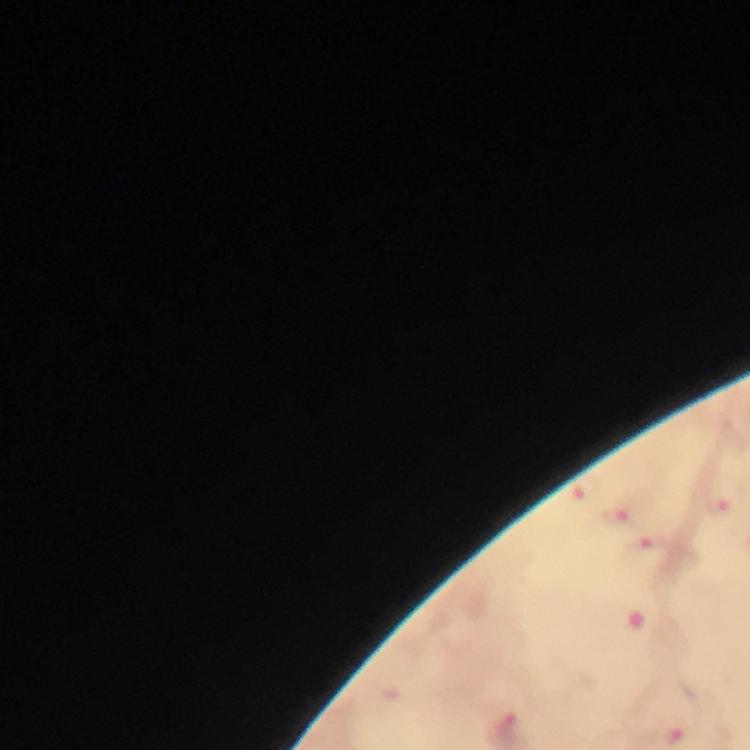
Approximate centers as (x, y) in pixels. Malaria parasite locations: (583, 490), (724, 507), (616, 516), (654, 548). Giemsa stain. Image is 750×750 pixels. Immersion oil was used. A crop from one field of view. From a diagnostic examination for malaria. Photographed with a smartphone mounted on the microscope. Thick blood film. At 100x magnification.